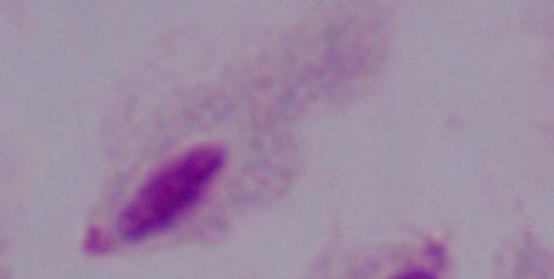

modality = micrograph
magnification = 1000x
identification = trichomonad